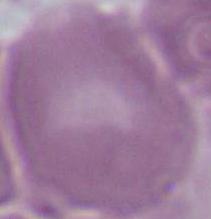
Photomicrograph. An erythrocyte is shown. 1000x magnification.